Assess the morphology of the erythrocytes.
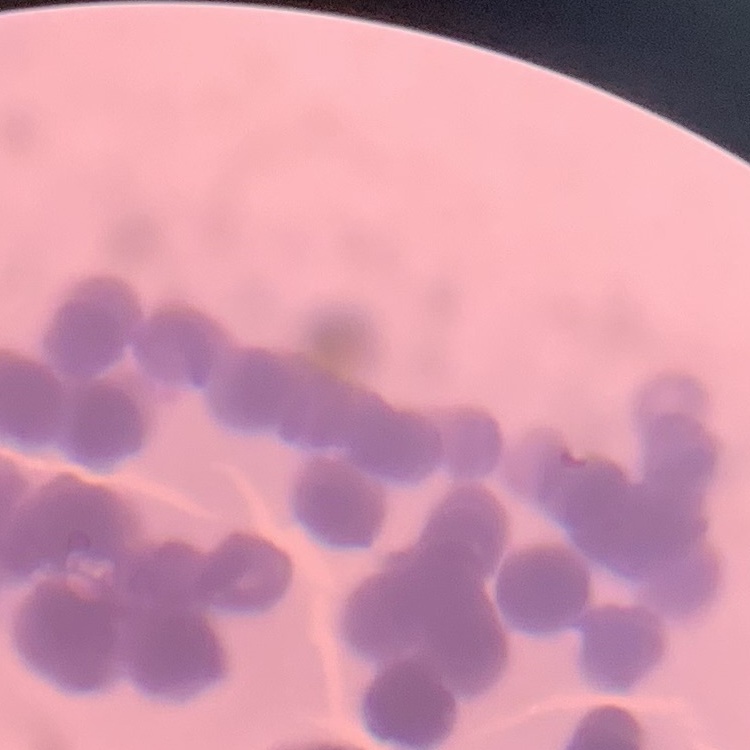
They show rouleaux formation.

image type = square crop of a larger photomicrograph
stain = Field's or Giemsa
preparation = thin peripheral smear